Classify this cell by malaria status.
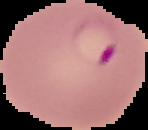
Parasitized.

image size = 148×130 pixels
preparation = thin blood smear
image type = segmented cell region with the area outside set to black